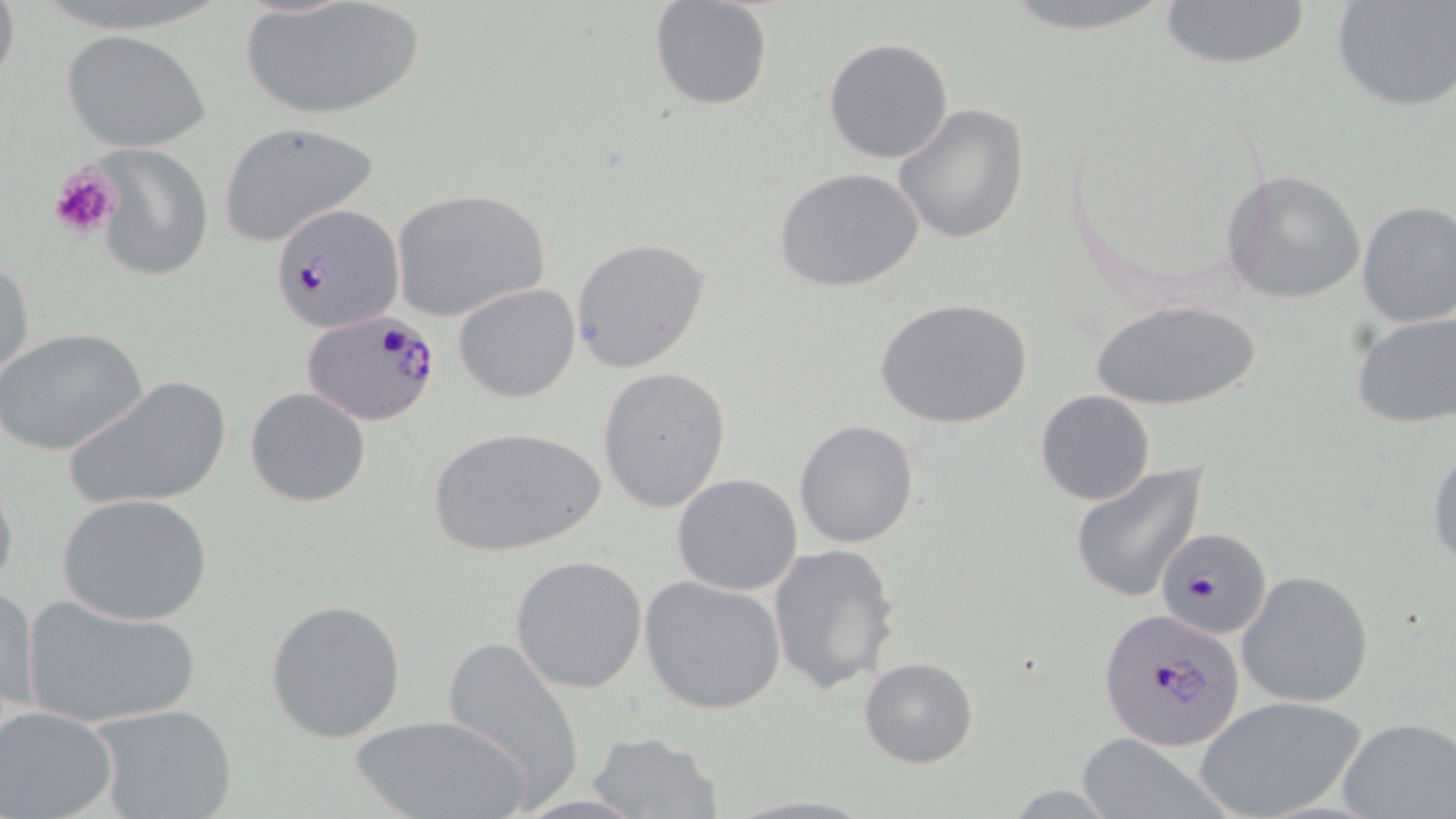 Approximate bounding boxes as named x1/y1/x2/y2 corners in pixels. Uninfected red blood cell locations: (x1=0, y1=0, x2=20, y2=98), (x1=238, y1=0, x2=426, y2=123), (x1=647, y1=0, x2=774, y2=112), (x1=989, y1=0, x2=1186, y2=34), (x1=1153, y1=0, x2=1316, y2=70), (x1=1331, y1=1, x2=1456, y2=113), (x1=63, y1=30, x2=210, y2=154), (x1=823, y1=37, x2=954, y2=164), (x1=893, y1=102, x2=1030, y2=245), (x1=217, y1=121, x2=379, y2=249), (x1=93, y1=145, x2=213, y2=279), (x1=773, y1=166, x2=925, y2=293), (x1=1221, y1=169, x2=1367, y2=305), (x1=389, y1=187, x2=552, y2=324), (x1=1356, y1=200, x2=1456, y2=327), (x1=570, y1=237, x2=712, y2=372), (x1=0, y1=254, x2=35, y2=386), (x1=452, y1=282, x2=581, y2=404), (x1=1088, y1=296, x2=1263, y2=413), (x1=877, y1=297, x2=1033, y2=431), (x1=1350, y1=310, x2=1456, y2=428), (x1=0, y1=326, x2=148, y2=455), (x1=597, y1=365, x2=731, y2=512), (x1=63, y1=374, x2=233, y2=511), (x1=244, y1=386, x2=371, y2=506), (x1=1035, y1=389, x2=1155, y2=505), (x1=794, y1=419, x2=920, y2=548), (x1=427, y1=425, x2=604, y2=558), (x1=1426, y1=437, x2=1456, y2=572), (x1=1069, y1=462, x2=1208, y2=603), (x1=0, y1=463, x2=20, y2=603), (x1=671, y1=473, x2=803, y2=593), (x1=58, y1=493, x2=214, y2=627), (x1=768, y1=543, x2=900, y2=695), (x1=509, y1=554, x2=649, y2=694), (x1=1236, y1=569, x2=1375, y2=709), (x1=640, y1=576, x2=787, y2=715), (x1=2, y1=581, x2=39, y2=723), (x1=22, y1=594, x2=200, y2=728), (x1=266, y1=598, x2=407, y2=742), (x1=438, y1=630, x2=587, y2=803), (x1=858, y1=656, x2=980, y2=769), (x1=1192, y1=693, x2=1368, y2=819), (x1=92, y1=704, x2=240, y2=819), (x1=0, y1=706, x2=119, y2=819), (x1=350, y1=711, x2=536, y2=819), (x1=1337, y1=717, x2=1456, y2=818), (x1=586, y1=730, x2=726, y2=819), (x1=1072, y1=735, x2=1227, y2=816). Plasmodium falciparum-infected red blood cell locations: (x1=271, y1=202, x2=405, y2=334), (x1=302, y1=310, x2=442, y2=425), (x1=1158, y1=524, x2=1275, y2=640), (x1=1097, y1=607, x2=1245, y2=752). Platelet locations: (x1=47, y1=163, x2=121, y2=240). Slide-level diagnosis: Plasmodium falciparum. May-Grünwald-Giemsa stain. Optical microscopy. 1000x magnification. Image is 1456×819 pixels. Thin blood smear. One field of a larger specimen.